Name the blood parasite species.
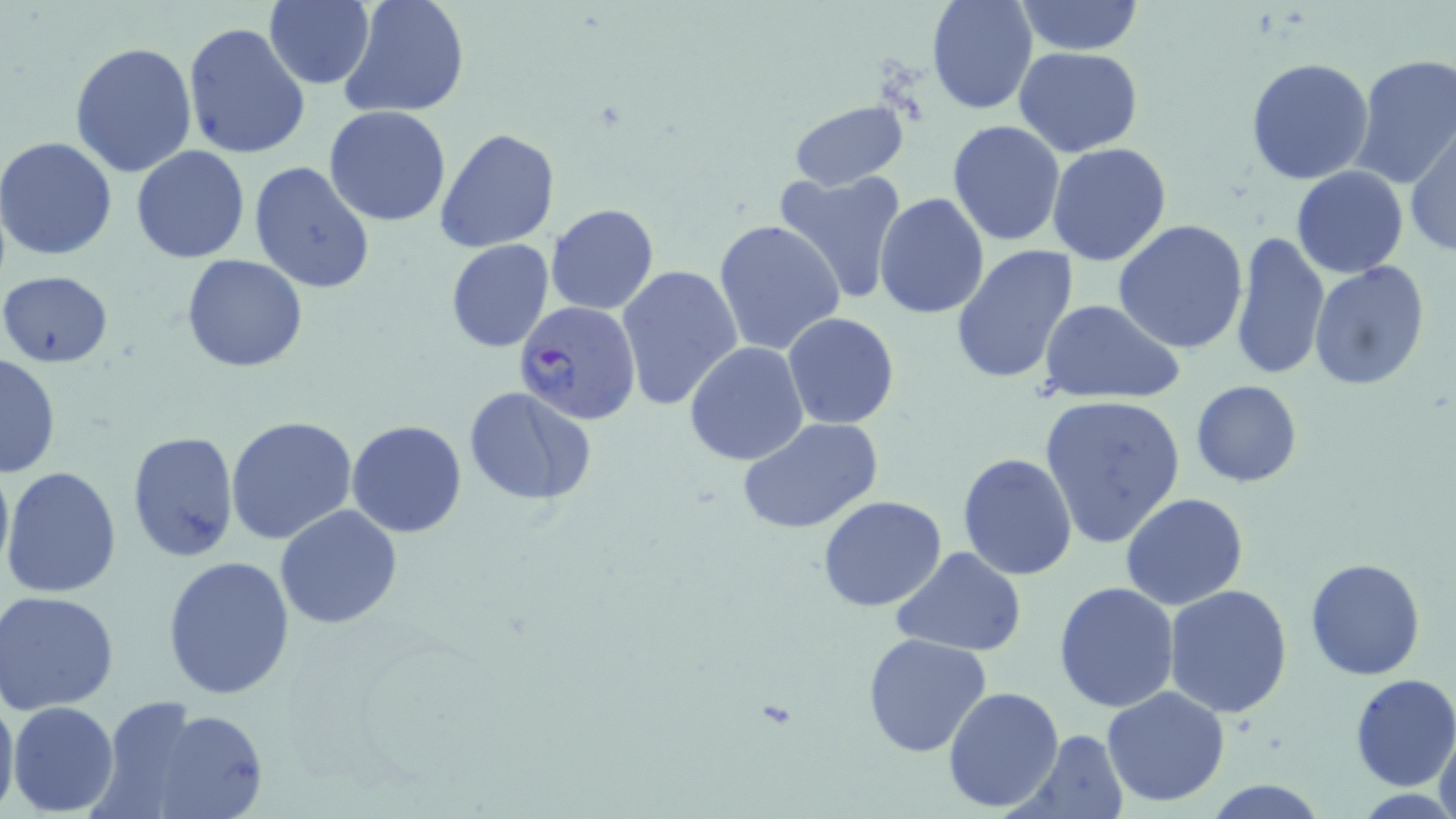
Plasmodium falciparum.

Approximate bounding boxes as (x1, y1, x2, y2) in pixels. Plasmodium falciparum-infected red blood cell locations: (511, 301, 641, 425). Uninfected red blood cell locations: (265, 0, 376, 89), (338, 0, 471, 119), (927, 0, 1036, 116), (1015, 0, 1145, 55), (182, 23, 310, 160), (70, 40, 197, 178), (1014, 46, 1143, 156), (1351, 53, 1456, 189), (1245, 57, 1376, 186), (789, 98, 910, 192), (324, 105, 452, 227), (947, 119, 1066, 247), (1405, 124, 1456, 258), (435, 128, 559, 253), (1, 136, 120, 260), (1047, 142, 1173, 266), (130, 146, 251, 263), (248, 162, 375, 293), (1291, 166, 1408, 278), (770, 167, 908, 305), (874, 191, 990, 320), (546, 203, 660, 315), (714, 219, 845, 358), (1115, 219, 1249, 355), (1230, 232, 1330, 380), (444, 239, 554, 353), (951, 244, 1079, 384), (181, 254, 308, 373), (1310, 262, 1430, 392), (615, 263, 744, 412), (1, 268, 114, 368), (1039, 299, 1186, 406), (783, 312, 900, 429), (684, 340, 811, 466), (1, 352, 61, 479), (1191, 380, 1302, 487), (462, 386, 595, 506), (1040, 393, 1186, 550), (344, 404, 592, 522), (225, 415, 357, 544), (737, 415, 887, 536), (347, 419, 468, 537), (127, 430, 240, 562), (252, 435, 387, 615), (957, 452, 1079, 580), (0, 453, 13, 584), (2, 467, 122, 597), (1120, 493, 1248, 610), (818, 495, 949, 611), (275, 505, 403, 630), (892, 548, 1024, 656), (163, 554, 297, 699), (1305, 557, 1428, 681), (1054, 582, 1180, 714), (1165, 586, 1294, 718), (1, 591, 119, 713), (863, 632, 993, 759), (1349, 674, 1456, 791), (942, 685, 1066, 813), (1101, 685, 1231, 807), (0, 690, 19, 819), (9, 701, 119, 816), (116, 702, 271, 819), (1431, 726, 1455, 818), (1012, 729, 1130, 819), (1202, 780, 1330, 818). Thin blood smear. One field of a larger specimen. Optical microscopy. 1000x magnification. Image is 1456×819 pixels. May-Grünwald-Giemsa stain.